Locate every Plasmodium parasite.
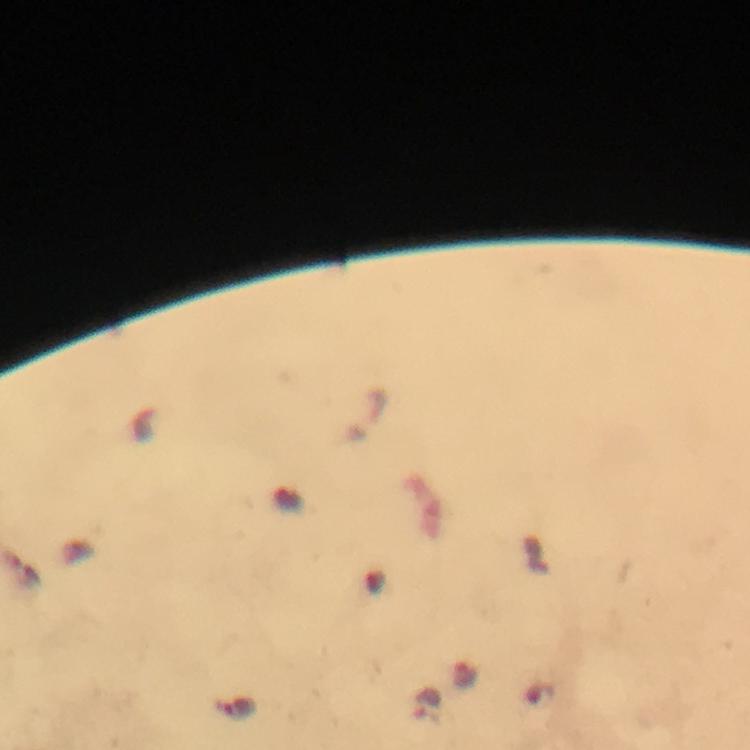

Approximate centers as {x, y} in pixels.
Plasmodium parasites: {427, 705}.

magnification = 100x
image size = 750×750 pixels
immersion oil = used
capture = smartphone camera through the microscope
context = from a malaria diagnostic workup
stain = Giemsa
preparation = thick blood film
cropped from = a single field of view